Outline each Trypanosoma brucei.
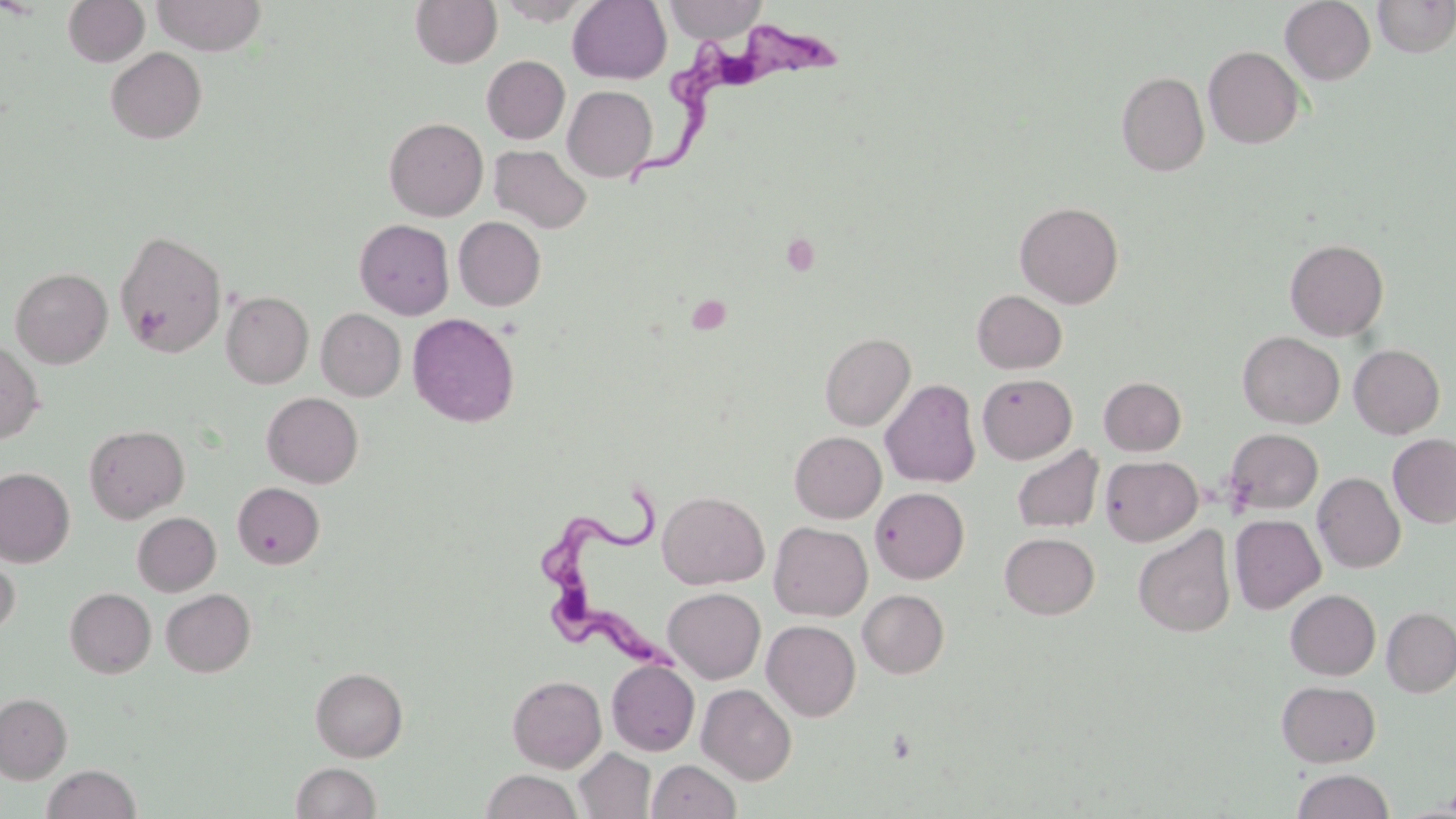
Approximate bounding boxes as named x1/y1/x2/y2 corners in pixels.
Trypanosoma brucei: (x1=618, y1=18, x2=854, y2=190), (x1=539, y1=483, x2=686, y2=679).

Uninfected red blood cell locations: (x1=62, y1=0, x2=149, y2=67), (x1=151, y1=0, x2=267, y2=55), (x1=410, y1=0, x2=502, y2=69), (x1=496, y1=0, x2=593, y2=25), (x1=567, y1=0, x2=671, y2=84), (x1=665, y1=0, x2=765, y2=43), (x1=1281, y1=0, x2=1375, y2=84), (x1=1372, y1=0, x2=1456, y2=58), (x1=1203, y1=46, x2=1305, y2=148), (x1=106, y1=47, x2=207, y2=143), (x1=482, y1=56, x2=570, y2=144), (x1=1116, y1=71, x2=1209, y2=177), (x1=562, y1=85, x2=657, y2=182), (x1=384, y1=117, x2=488, y2=220), (x1=490, y1=145, x2=592, y2=233), (x1=1015, y1=201, x2=1124, y2=309), (x1=454, y1=216, x2=546, y2=310), (x1=355, y1=219, x2=454, y2=319), (x1=114, y1=229, x2=227, y2=358), (x1=1285, y1=239, x2=1388, y2=340), (x1=10, y1=267, x2=112, y2=368), (x1=972, y1=290, x2=1067, y2=374), (x1=221, y1=291, x2=313, y2=388), (x1=317, y1=309, x2=405, y2=401), (x1=407, y1=312, x2=520, y2=427), (x1=1237, y1=331, x2=1344, y2=428), (x1=819, y1=332, x2=915, y2=430), (x1=0, y1=340, x2=44, y2=443), (x1=1349, y1=344, x2=1445, y2=439), (x1=977, y1=374, x2=1077, y2=464), (x1=1098, y1=376, x2=1186, y2=456), (x1=880, y1=379, x2=981, y2=488), (x1=262, y1=392, x2=363, y2=488), (x1=84, y1=424, x2=190, y2=523), (x1=1224, y1=428, x2=1323, y2=516), (x1=790, y1=431, x2=886, y2=522), (x1=1388, y1=434, x2=1456, y2=527), (x1=1011, y1=445, x2=1104, y2=533), (x1=1100, y1=455, x2=1202, y2=546), (x1=0, y1=467, x2=75, y2=567), (x1=1313, y1=472, x2=1405, y2=573), (x1=232, y1=482, x2=324, y2=568), (x1=870, y1=487, x2=969, y2=583), (x1=657, y1=491, x2=769, y2=589), (x1=132, y1=512, x2=221, y2=596), (x1=1230, y1=514, x2=1325, y2=614), (x1=769, y1=522, x2=872, y2=621), (x1=1133, y1=525, x2=1236, y2=637), (x1=999, y1=533, x2=1100, y2=619), (x1=0, y1=546, x2=20, y2=639), (x1=663, y1=587, x2=765, y2=684), (x1=65, y1=588, x2=156, y2=677), (x1=161, y1=588, x2=255, y2=677), (x1=858, y1=589, x2=949, y2=678), (x1=1286, y1=589, x2=1380, y2=679), (x1=1382, y1=607, x2=1456, y2=697), (x1=762, y1=620, x2=860, y2=721), (x1=607, y1=660, x2=699, y2=756), (x1=310, y1=667, x2=408, y2=761), (x1=507, y1=675, x2=606, y2=772), (x1=1276, y1=680, x2=1381, y2=767), (x1=697, y1=684, x2=796, y2=784), (x1=0, y1=693, x2=71, y2=782), (x1=11, y1=728, x2=95, y2=791), (x1=575, y1=748, x2=656, y2=818), (x1=647, y1=759, x2=741, y2=819), (x1=291, y1=761, x2=382, y2=819), (x1=41, y1=765, x2=142, y2=818), (x1=481, y1=769, x2=582, y2=819), (x1=1291, y1=769, x2=1395, y2=819). Platelet locations: (x1=687, y1=294, x2=732, y2=334). Slide-level diagnosis: Trypanosoma brucei. One field of a larger specimen. May-Grünwald-Giemsa stain. 1000x magnification. Thin blood smear. Optical microscopy. Image is 1456×819 pixels.